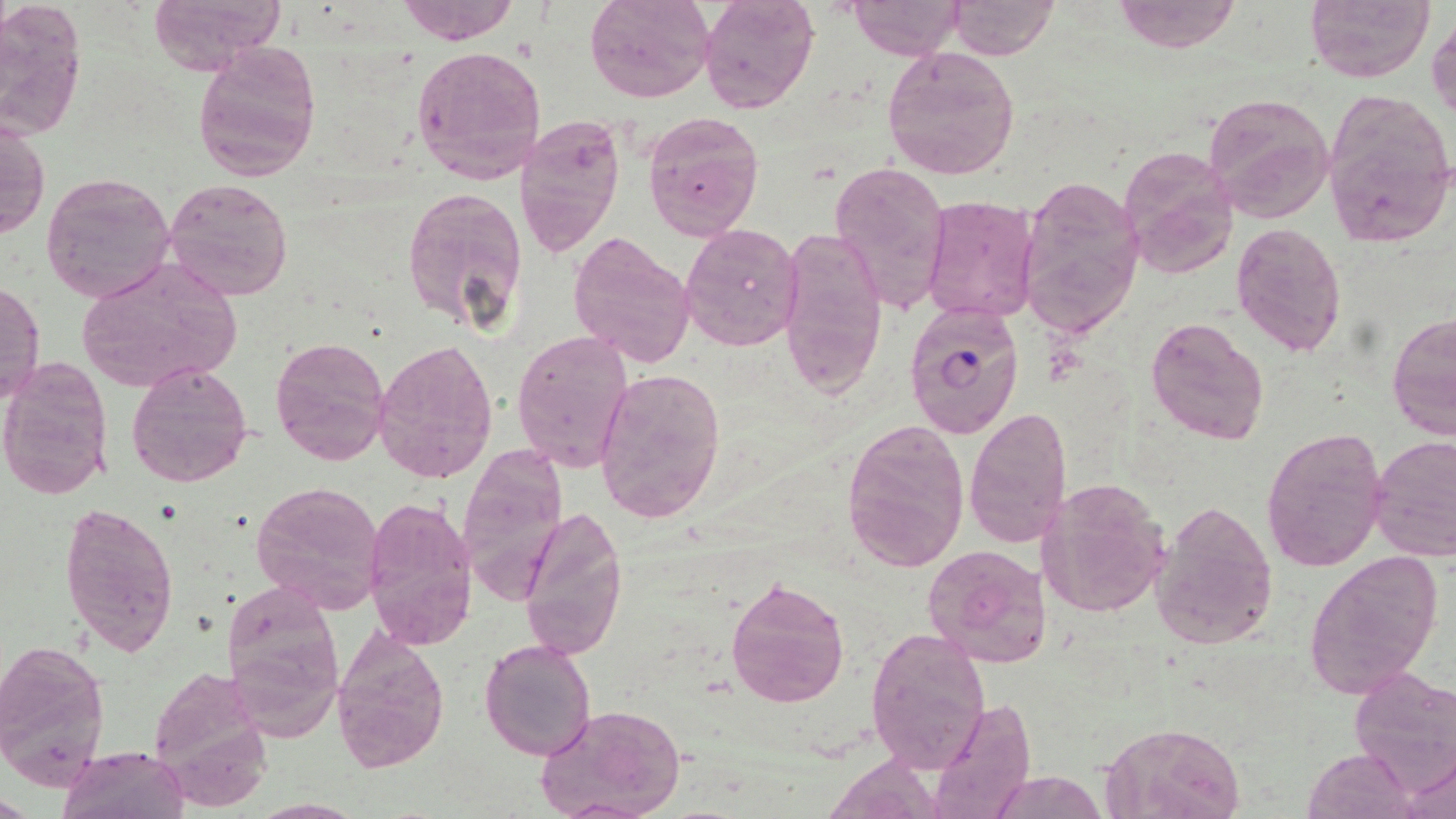

Approximate bounding boxes as (x1,y1)-(x2,y2) corner pairs in pixels. Plasmodium falciparum-infected red blood cell locations: (904,302)-(1025,440). Uninfected red blood cell locations: (147,0)-(287,74), (395,0)-(520,45), (584,0)-(714,103), (697,0)-(818,112), (847,0)-(964,58), (948,0)-(1057,58), (1113,0)-(1242,53), (1306,0)-(1435,82), (0,3)-(87,141), (1428,15)-(1456,123), (192,39)-(323,181), (410,43)-(547,186), (882,45)-(1021,180), (1204,91)-(1333,225), (1323,93)-(1456,246), (643,111)-(764,240), (515,114)-(626,258), (1,117)-(49,242), (1118,146)-(1241,278), (826,157)-(950,317), (40,170)-(175,303), (1016,174)-(1145,338), (163,178)-(294,301), (402,185)-(528,333), (919,194)-(1041,326), (1230,222)-(1346,358), (679,223)-(803,353), (775,229)-(889,400), (567,231)-(696,368), (74,256)-(241,397), (1,281)-(45,404), (1387,312)-(1456,440), (1145,316)-(1270,445), (512,328)-(633,471), (270,335)-(393,467), (372,340)-(499,485), (0,357)-(114,500), (126,360)-(253,487), (594,367)-(726,523), (965,405)-(1072,548), (839,419)-(970,573), (1260,427)-(1389,572), (1370,435)-(1456,561), (456,448)-(568,608), (1035,475)-(1172,618), (252,480)-(386,612), (361,495)-(478,651), (1150,499)-(1278,649), (60,500)-(181,656), (519,505)-(628,661), (922,543)-(1055,668), (1304,551)-(1444,697), (725,576)-(850,708), (220,583)-(340,728), (330,624)-(450,774), (865,627)-(992,774), (0,636)-(113,787), (480,636)-(597,760), (146,668)-(270,810), (1350,668)-(1456,788), (927,697)-(1037,819), (536,702)-(687,819), (1099,720)-(1246,819), (58,744)-(187,819), (1304,747)-(1417,819), (1404,754)-(1456,817), (994,772)-(1101,817), (246,798)-(369,818). Slide-level diagnosis: Plasmodium falciparum. Image is 1456×819 pixels. Thin blood film. May-Grünwald-Giemsa-stained preparation. 1000x magnification. One field of a larger specimen. Optical microscopy.